Name the blood parasite species.
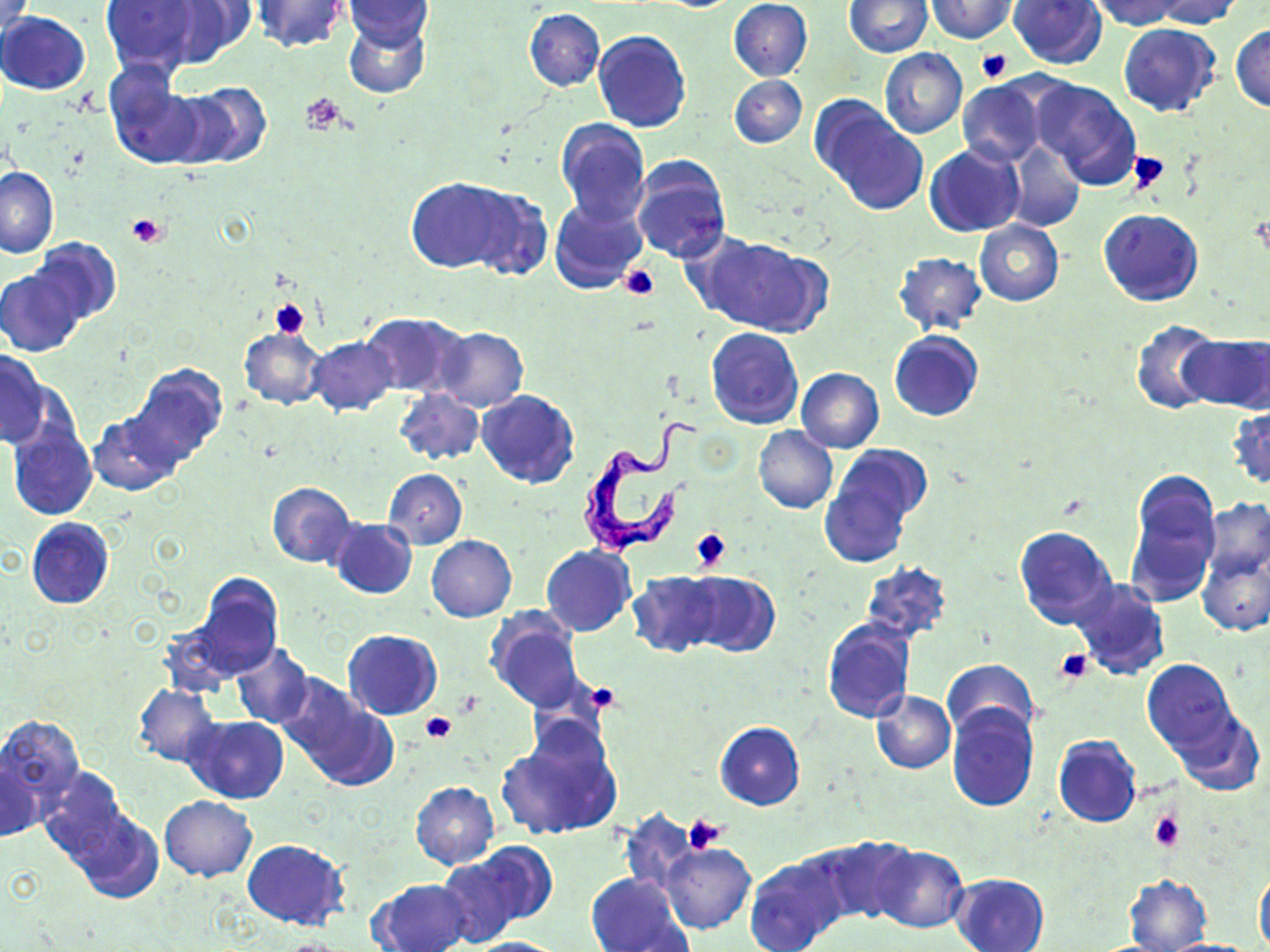

Trypanosoma brucei.

image size = 1270×952 pixels
platelet locations = approximate bounding boxes as (x1,y1)-(x2,y2) corner pairs in pixels: (976,49)-(1012,84), (301,93)-(346,133), (1128,151)-(1170,195), (127,214)-(168,249), (620,264)-(659,301), (270,297)-(312,340), (690,528)-(732,572), (1055,649)-(1094,685), (588,681)-(622,714), (456,691)-(483,717), (422,711)-(456,743), (1148,810)-(1185,852), (682,812)-(727,852)
modality = light microscopy
field of view = single
uninfected red blood cell locations = approximate bounding boxes as (x1,y1)-(x2,y2) corner pairs in pixels: (100,0)-(200,76), (155,0)-(257,68), (1008,0)-(1107,68), (1086,0)-(1185,31), (1150,0)-(1247,29), (248,1)-(350,54), (342,1)-(435,49), (728,1)-(813,81), (925,1)-(1020,42), (843,2)-(932,57), (524,9)-(605,91), (0,12)-(90,95), (344,18)-(429,99), (1117,22)-(1221,117), (1231,23)-(1270,114), (593,30)-(691,133), (880,47)-(968,138), (102,64)-(206,169), (730,75)-(806,148), (1030,76)-(1142,191), (956,79)-(1048,167), (175,83)-(272,168), (812,97)-(926,215), (556,118)-(651,225), (1003,140)-(1086,233), (925,144)-(1024,237), (631,156)-(731,263), (0,166)-(58,257), (406,176)-(519,273), (464,185)-(553,282), (549,196)-(648,293), (1099,209)-(1204,307), (974,220)-(1063,305), (28,237)-(121,326), (697,237)-(826,337), (893,252)-(988,336), (0,268)-(83,357), (361,312)-(467,398), (1131,318)-(1220,415), (237,325)-(326,410), (706,325)-(803,429), (434,327)-(529,410), (889,331)-(984,421), (1181,334)-(1270,412), (307,337)-(398,416), (1,348)-(49,449), (127,363)-(228,466), (796,367)-(884,453), (394,388)-(484,466), (477,390)-(579,487), (1227,405)-(1270,490), (89,412)-(182,496), (8,419)-(97,521), (753,426)-(838,514), (829,443)-(932,529), (818,465)-(915,569), (382,468)-(467,549), (1126,469)-(1221,604), (267,482)-(355,568), (1201,499)-(1270,580), (26,517)-(115,609), (328,518)-(417,598), (1015,525)-(1119,629), (427,534)-(517,621), (541,544)-(636,636), (1198,552)-(1270,636), (860,560)-(953,644), (681,571)-(780,658), (629,572)-(722,657), (187,573)-(283,680), (1071,580)-(1169,679), (487,608)-(586,712), (821,617)-(916,725), (342,629)-(442,720), (231,642)-(314,728), (1142,658)-(1237,755), (943,659)-(1038,740), (277,676)-(394,790), (132,685)-(221,767), (871,691)-(956,774), (947,705)-(1038,811), (1173,707)-(1263,796), (183,715)-(289,803), (0,716)-(86,809), (495,719)-(623,842), (714,721)-(805,810), (1053,735)-(1141,827), (1,758)-(42,842), (38,767)-(133,864), (409,781)-(500,869), (160,795)-(256,882), (65,808)-(163,902), (619,811)-(701,897), (811,836)-(916,926), (241,839)-(348,929), (659,842)-(756,933), (871,844)-(967,934), (435,853)-(538,947), (744,855)-(846,952), (1255,867)-(1270,950), (584,872)-(692,952), (949,873)-(1049,952), (1123,875)-(1212,951), (368,878)-(474,952), (463,936)-(569,952), (1156,938)-(1259,951)
Trypanosoma brucei locations = approximate bounding boxes as (x1,y1)-(x2,y2) corner pairs in pixels: (581,402)-(699,558)
stain = May-Grünwald-Giemsa
preparation = thin blood film
magnification = 1000x